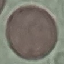

Result: negative for malaria parasites. Cell patch, automatically extracted from a larger field of view and resized to 64 × 64 pixels. Photographed with a smartphone camera at the microscope eyepiece. Giemsa-stained preparation. Thin blood smear.